Classify this cell by malaria status.
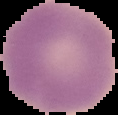
Uninfected.

{
  "image_type": "segmented cell region on a black background",
  "preparation": "thin blood smear",
  "image_size": "118×115 pixels"
}